Assess for parasitized red blood cells.
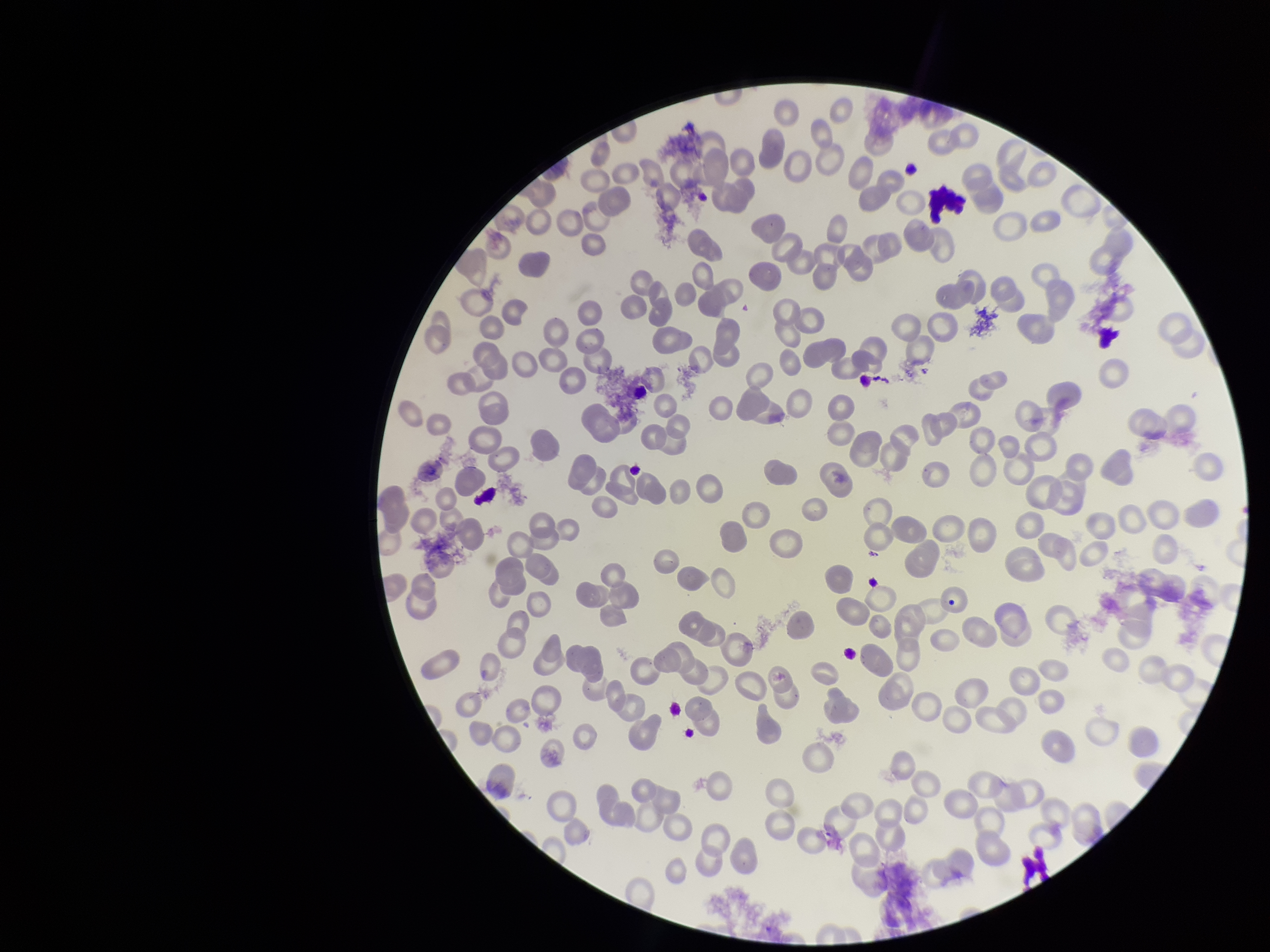

None identified.

field of view = single
stain = Giemsa
image size = 1270×952 pixels
preparation = thin blood smear
red blood cell count = 199
patient malaria status = negative
capture = smartphone photograph through the microscope eyepiece
parasitized red blood cell count = 0